Identify the parasite.
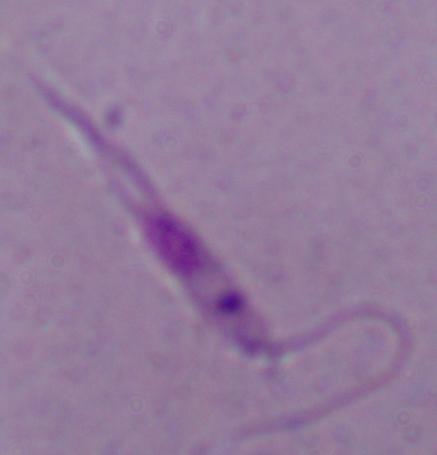
This is Leishmania.

Captured at 1000x magnification. Micrograph.